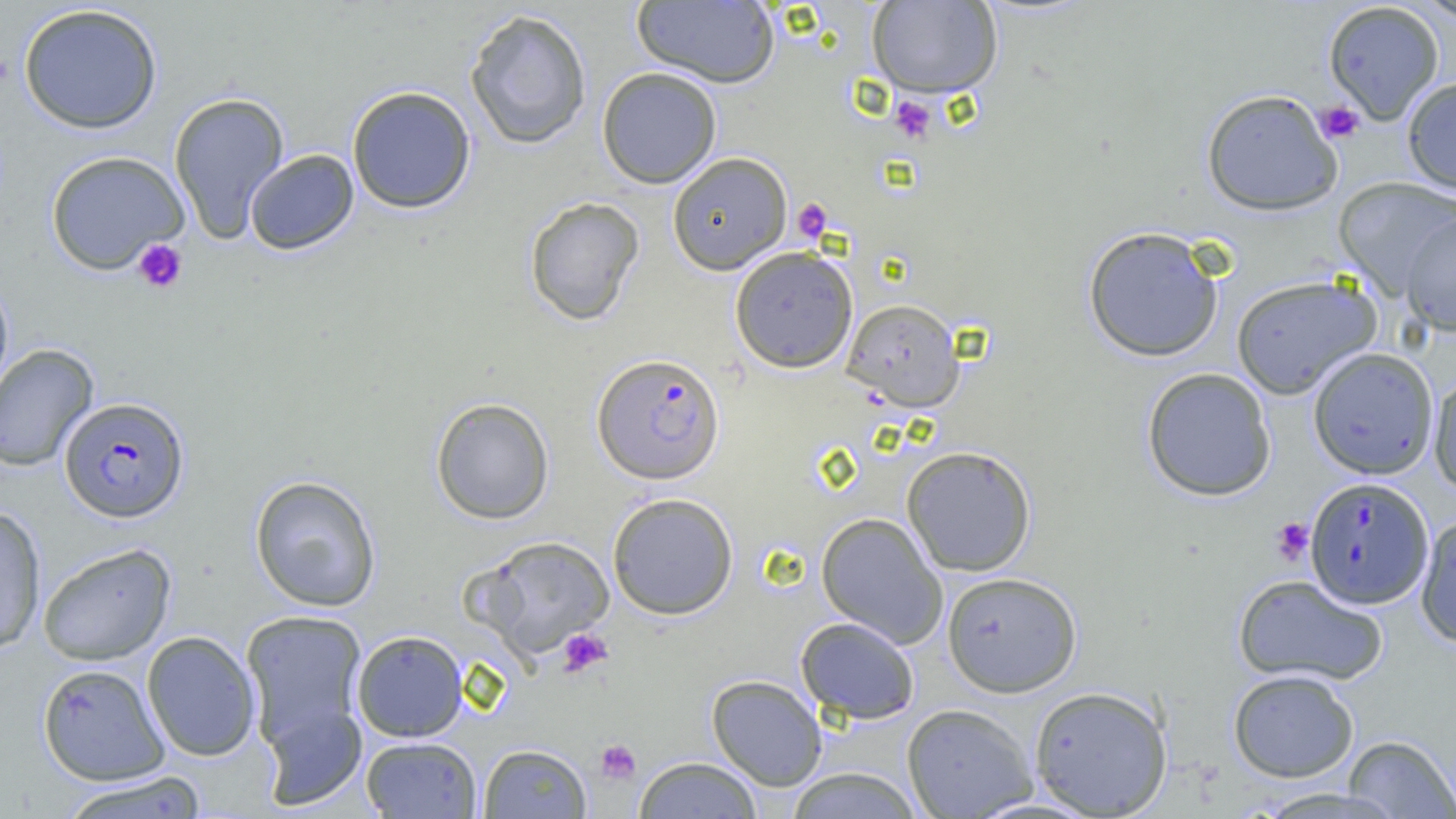

Summary:
  - Coordinate format: approximate bounding boxes as (x1, y1, x2, y2) in pixels
  - Uninfected red blood cell locations: (632, 0, 779, 87), (867, 0, 1003, 98), (1411, 0, 1455, 24), (1323, 2, 1445, 124), (17, 3, 163, 134), (464, 7, 592, 150), (596, 66, 722, 188), (1402, 77, 1456, 196), (346, 85, 477, 214), (1200, 88, 1343, 216), (169, 91, 290, 244), (245, 149, 359, 255), (45, 150, 190, 275), (667, 152, 792, 274), (1333, 177, 1456, 298), (524, 197, 644, 326), (1400, 210, 1456, 337), (1082, 226, 1224, 362), (729, 246, 858, 373), (1231, 273, 1382, 399), (0, 276, 14, 402), (842, 298, 965, 412), (0, 343, 100, 472), (1307, 347, 1440, 480), (1140, 367, 1277, 502), (1428, 371, 1456, 496), (430, 397, 555, 525), (901, 445, 1037, 576), (248, 474, 382, 612), (607, 492, 739, 619), (0, 504, 47, 654), (815, 512, 948, 647), (1416, 512, 1456, 650), (473, 535, 616, 660), (37, 542, 176, 666), (941, 571, 1083, 697), (1232, 574, 1389, 686), (240, 610, 368, 749), (794, 616, 920, 724), (351, 630, 468, 742), (142, 631, 261, 761), (37, 663, 170, 785), (1227, 668, 1359, 783), (706, 674, 827, 791), (1028, 685, 1173, 817), (259, 701, 368, 811), (901, 703, 1038, 818), (1342, 734, 1456, 818), (361, 736, 482, 818), (478, 744, 591, 818), (633, 756, 764, 818), (785, 767, 924, 818), (56, 771, 210, 819), (1249, 786, 1408, 819)
  - Platelet locations: (889, 96, 936, 143), (1315, 100, 1365, 143), (792, 199, 833, 243), (132, 238, 188, 294), (1271, 517, 1314, 565), (556, 627, 612, 678), (594, 739, 640, 785)
  - Plasmodium falciparum-infected red blood cell locations: (592, 353, 725, 484), (59, 396, 190, 522), (1305, 476, 1434, 608)
  - Slide-level diagnosis: Plasmodium falciparum
  - Preparation: thin blood smear
  - Field of view: one of a larger specimen
  - Magnification: 1000x
  - Modality: light microscopy
  - Image size: 1456×819 pixels